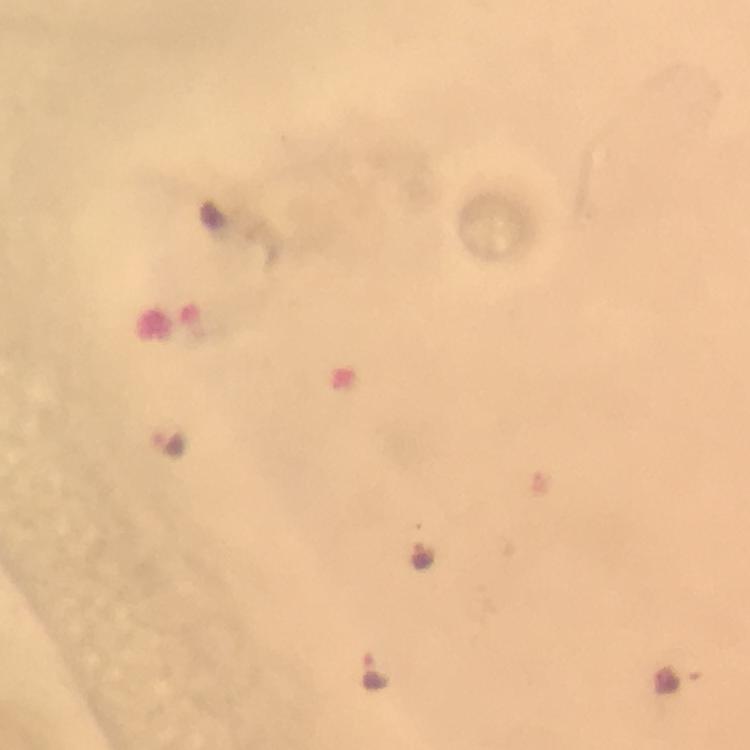
Approximate object centers, in pixels from the top-left corner.
Summary:
  - Malaria parasite locations: (x=170, y=443), (x=422, y=557), (x=375, y=672)
  - Immersion oil: applied
  - Preparation: thick smear
  - Capture: smartphone photograph through a microscope
  - Context: from a malaria diagnostic workup
  - Cropped from: a single field of view
  - Image size: 750×750 pixels
  - Stain: Giemsa
  - Magnification: 100x